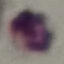 Result: no malaria parasites seen. Cell patch, automatically extracted from a larger field of view and resized to 64 × 64 pixels. Photographed with a smartphone camera at the microscope eyepiece. Giemsa stain. Thin blood smear.